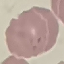 Result: malaria parasites identified. Acquired by smartphone through the microscope eyepiece. Cell patch, automatically extracted from a larger field of view and resized to 64 × 64 pixels. Giemsa stain. Thin smear of blood.